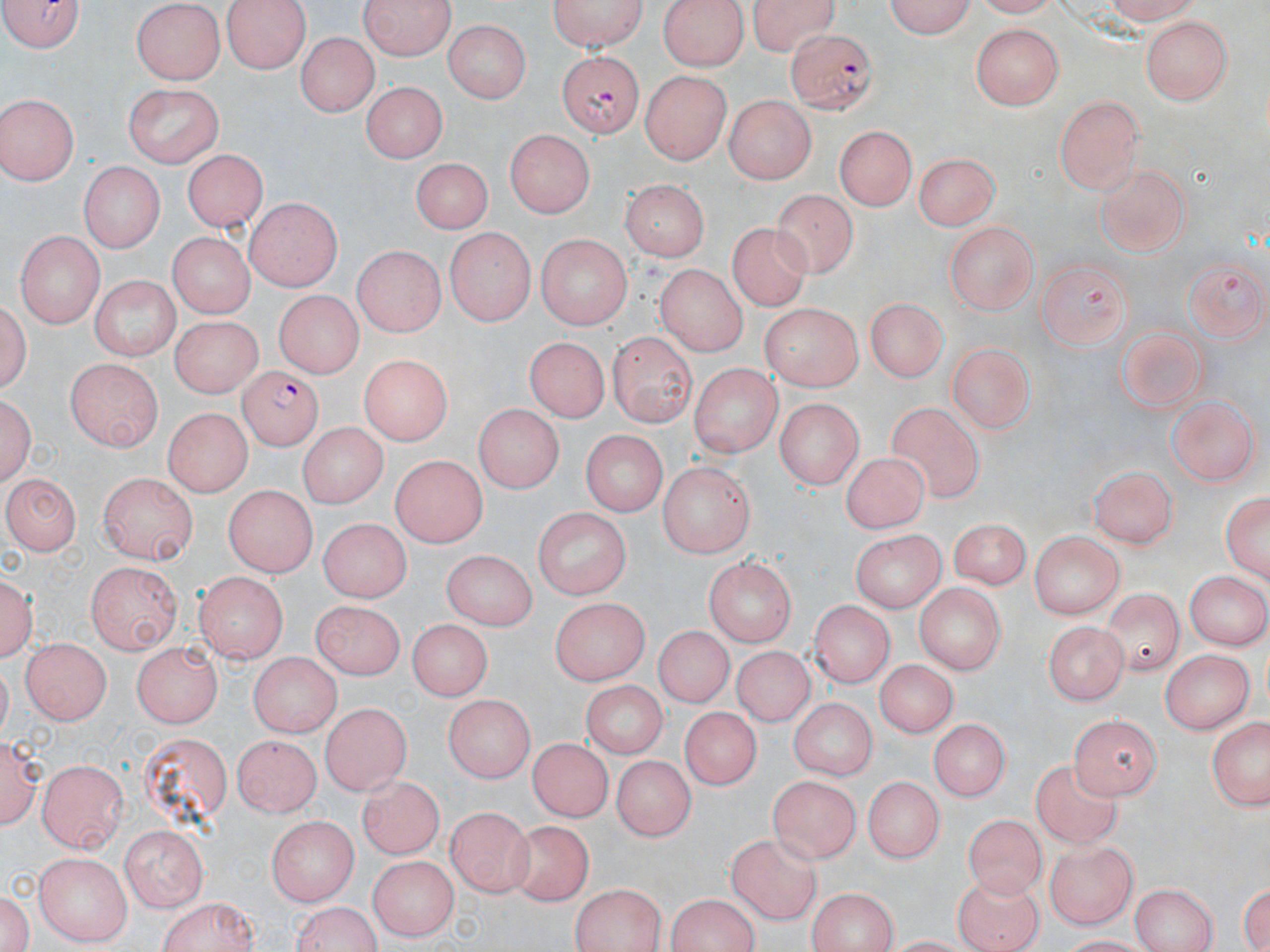

Summary:
  - Coordinate format: approximate bounding boxes as [x1, y1, x2, y2] in pixels
  - Uninfected red blood cell locations: [2, 0, 87, 56], [221, 0, 309, 73], [360, 0, 458, 61], [546, 0, 649, 52], [657, 0, 749, 72], [745, 0, 844, 54], [878, 0, 975, 37], [1095, 0, 1205, 23], [132, 2, 227, 84], [1142, 17, 1233, 105], [445, 20, 529, 104], [970, 24, 1065, 111], [298, 32, 378, 115], [319, 51, 436, 136], [640, 69, 732, 165], [361, 79, 446, 164], [124, 83, 226, 167], [1056, 93, 1146, 194], [725, 94, 814, 184], [0, 95, 80, 186], [836, 127, 916, 209], [506, 128, 592, 219], [184, 148, 267, 230], [915, 149, 1002, 232], [407, 158, 495, 233], [76, 162, 163, 252], [1095, 164, 1194, 258], [620, 177, 712, 262], [776, 189, 857, 277], [241, 199, 339, 290], [729, 223, 812, 315], [943, 224, 1039, 312], [445, 229, 533, 325], [14, 231, 103, 328], [164, 233, 255, 319], [536, 234, 629, 330], [354, 246, 447, 337], [1185, 257, 1267, 339], [1033, 259, 1133, 346], [656, 262, 752, 357], [89, 275, 180, 358], [272, 291, 363, 378], [2, 296, 33, 400], [866, 296, 948, 379], [761, 303, 864, 389], [167, 314, 258, 396], [1114, 320, 1211, 414], [610, 328, 697, 427], [525, 333, 612, 422], [947, 341, 1037, 435], [357, 355, 454, 444], [66, 358, 165, 449], [689, 364, 781, 460], [1, 389, 37, 491], [1169, 395, 1258, 488], [772, 397, 867, 486], [888, 400, 984, 505], [474, 405, 560, 496], [164, 409, 248, 495], [295, 422, 388, 509], [584, 428, 669, 514], [390, 451, 486, 548], [837, 452, 928, 534], [1091, 461, 1178, 547], [659, 462, 756, 557], [100, 471, 197, 565], [3, 474, 79, 555], [1222, 485, 1269, 587], [219, 486, 317, 579], [534, 508, 629, 602], [946, 516, 1030, 591], [320, 521, 411, 604], [851, 529, 946, 612], [1031, 534, 1126, 621], [440, 550, 541, 630], [703, 556, 798, 643], [87, 562, 181, 655], [2, 567, 36, 663], [1182, 569, 1268, 650], [198, 572, 286, 663], [916, 583, 1004, 678], [1098, 589, 1186, 678], [549, 595, 645, 682], [809, 596, 891, 686], [310, 602, 408, 683], [407, 622, 489, 703], [1044, 623, 1131, 703], [652, 625, 736, 706], [19, 637, 111, 725], [131, 642, 222, 727], [733, 643, 815, 724], [1162, 649, 1253, 736], [247, 653, 343, 737], [872, 658, 960, 737], [580, 679, 667, 757], [444, 695, 531, 782], [789, 697, 873, 780], [319, 702, 411, 795], [679, 707, 769, 797], [1071, 711, 1164, 796], [932, 716, 1008, 799], [1205, 719, 1270, 813], [136, 731, 237, 826], [231, 735, 323, 816], [2, 736, 41, 832], [527, 739, 612, 822], [615, 751, 692, 841], [38, 762, 129, 848], [1033, 762, 1133, 848], [774, 774, 861, 857], [359, 776, 447, 861], [865, 778, 940, 863], [449, 805, 533, 892], [964, 810, 1044, 894], [264, 814, 357, 903], [507, 826, 596, 906], [119, 828, 206, 913], [725, 835, 830, 923], [1044, 840, 1140, 931], [35, 853, 130, 944], [369, 858, 457, 939], [1237, 873, 1270, 952], [954, 876, 1045, 952], [1128, 882, 1222, 952], [570, 885, 669, 951], [2, 889, 33, 952], [804, 889, 900, 952], [151, 896, 261, 952], [663, 896, 765, 951], [289, 902, 383, 952]
  - Plasmodium falciparum-infected red blood cell locations: [786, 28, 878, 112], [556, 49, 643, 138], [237, 369, 325, 451]
  - Slide-level diagnosis: Plasmodium falciparum
  - Image size: 1270×952 pixels
  - Modality: optical microscopy
  - Magnification: 1000x
  - Stain: May-Grünwald-Giemsa
  - Field of view: single
  - Preparation: thin blood film